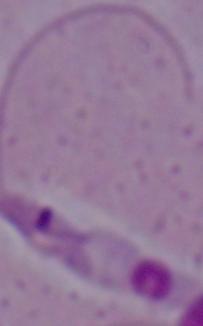

Summary:
  - Identification: Leishmania
  - Modality: micrograph
  - Magnification: 1000x